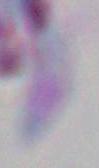

Toxoplasma gondii is seen. 1000x magnification. Photomicrograph.